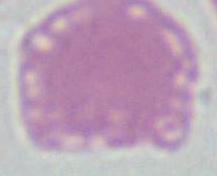

Summary:
  - Magnification: 1000x
  - Modality: micrograph
  - Identification: erythrocyte